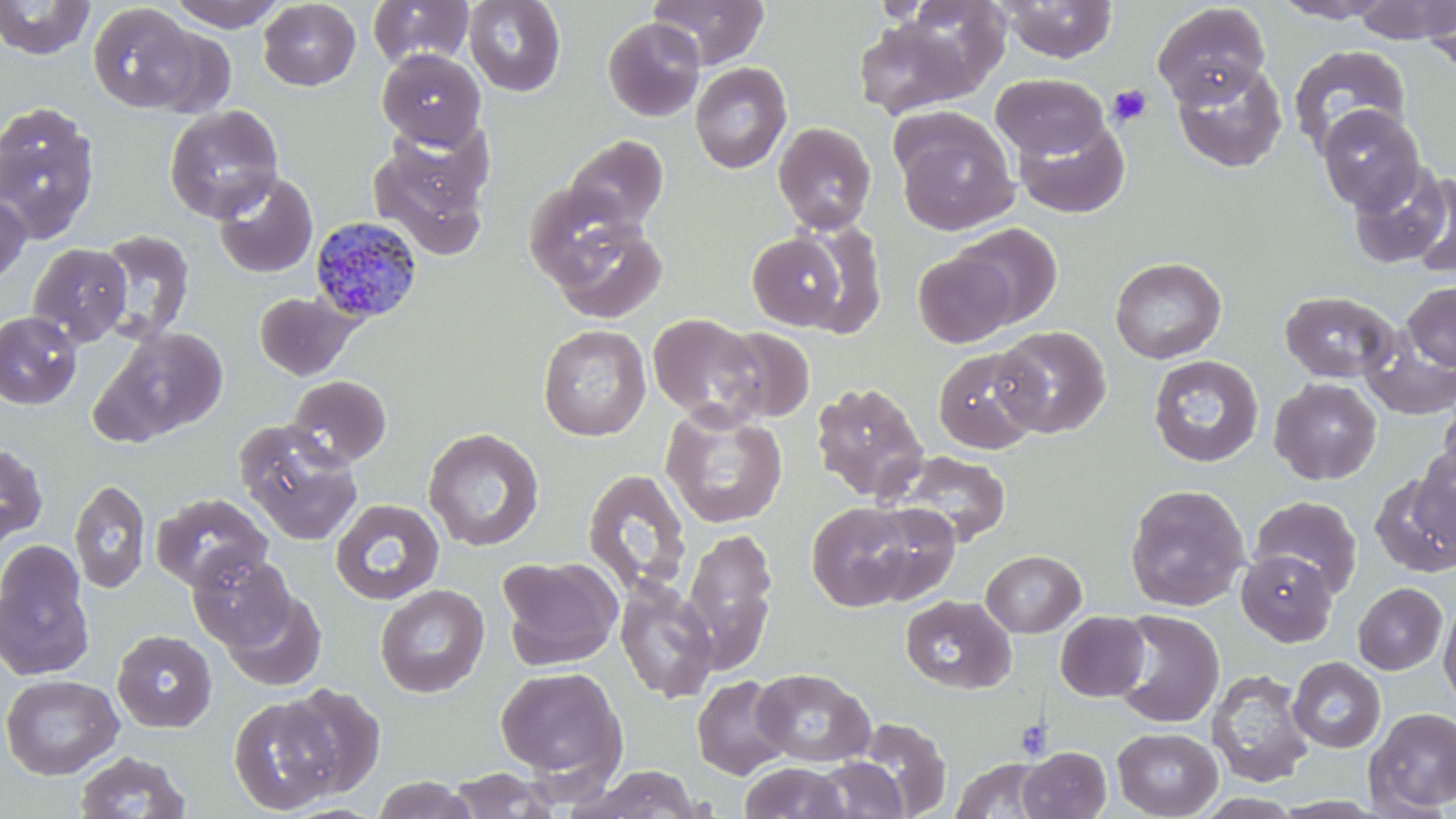
Approximate bounding boxes as (x1, y1, x2, y2) in pixels. Platelet locations: (1107, 84, 1152, 128), (1015, 718, 1052, 760). Plasmodium malariae-infected red blood cell locations: (309, 216, 425, 325). Uninfected red blood cell locations: (0, 0, 95, 60), (169, 0, 283, 28), (647, 0, 769, 69), (998, 0, 1118, 63), (1269, 0, 1396, 23), (1352, 0, 1455, 44), (1421, 0, 1455, 71), (258, 1, 361, 91), (368, 1, 474, 69), (464, 1, 566, 96), (87, 3, 202, 113), (1152, 3, 1271, 107), (853, 16, 976, 119), (602, 17, 705, 121), (139, 25, 237, 118), (1288, 44, 1412, 157), (377, 49, 486, 151), (1172, 61, 1287, 173), (689, 62, 793, 174), (991, 73, 1109, 160), (0, 101, 101, 244), (164, 105, 284, 223), (1317, 105, 1425, 214), (893, 114, 1018, 235), (1013, 117, 1129, 218), (773, 121, 876, 234), (367, 127, 493, 259), (563, 134, 668, 234), (1346, 160, 1454, 270), (213, 171, 318, 279), (1406, 171, 1456, 279), (522, 182, 644, 293), (0, 191, 30, 287), (548, 215, 667, 323), (787, 221, 888, 335), (951, 222, 1063, 329), (94, 228, 195, 344), (746, 232, 851, 331), (27, 242, 132, 346), (913, 251, 1016, 348), (1110, 256, 1227, 363), (1402, 281, 1456, 371), (254, 290, 360, 380), (1279, 290, 1399, 383), (0, 312, 82, 409), (647, 313, 767, 427), (537, 324, 651, 441), (99, 325, 230, 442), (992, 325, 1111, 438), (1360, 326, 1456, 420), (714, 327, 815, 423), (933, 346, 1045, 454), (1148, 354, 1264, 467), (288, 375, 392, 467), (1269, 377, 1382, 485), (810, 382, 928, 503), (1438, 397, 1456, 484), (661, 406, 788, 528), (234, 421, 364, 545), (423, 427, 545, 552), (0, 441, 48, 548), (1415, 443, 1455, 548), (892, 451, 1011, 547), (583, 468, 691, 596), (1371, 473, 1456, 577), (70, 478, 151, 596), (1124, 483, 1250, 611), (151, 493, 272, 593), (1249, 494, 1363, 597), (330, 498, 444, 604), (806, 500, 923, 612), (859, 502, 960, 605), (683, 527, 778, 672), (0, 542, 93, 680), (980, 549, 1086, 637), (1236, 549, 1337, 646), (189, 551, 295, 650), (496, 556, 623, 670), (615, 576, 719, 703), (1353, 582, 1448, 675), (375, 584, 490, 698), (221, 589, 326, 692), (1438, 594, 1456, 712), (900, 595, 1016, 694), (1112, 609, 1225, 728), (1055, 611, 1151, 701), (112, 630, 218, 732), (1288, 657, 1386, 753), (494, 665, 628, 786), (752, 668, 875, 768), (1206, 668, 1315, 787), (1, 674, 124, 779), (692, 675, 792, 780), (280, 683, 385, 798), (229, 695, 342, 814), (1364, 706, 1456, 815), (854, 718, 952, 818), (1112, 727, 1223, 818), (1018, 746, 1111, 818), (74, 750, 191, 819), (950, 757, 1055, 818), (810, 759, 909, 819), (739, 762, 852, 819), (578, 765, 706, 818), (445, 768, 564, 818), (372, 775, 477, 818). Slide-level diagnosis: Plasmodium malariae. May-Grünwald-Giemsa-stained preparation. 1000x magnification. Light microscopy. Image is 1456×819 pixels. Thin blood smear. One field of a larger specimen.